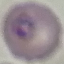
{
  "malaria_status": "parasitized",
  "stain": "Giemsa",
  "capture": "smartphone camera at the microscope eyepiece",
  "preparation": "thin blood smear",
  "image_type": "cell patch, automatically extracted from a larger field of view and resized to 64 × 64 pixels"
}